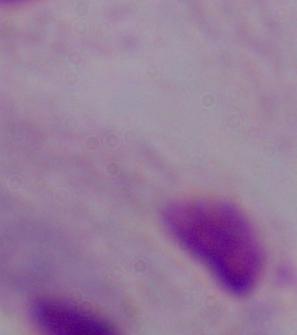
Summary:
  - Modality: micrograph
  - Identification: trichomonad
  - Magnification: 1000x